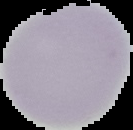
Summary:
  - Preparation: thin blood film
  - Image size: 133×130 pixels
  - Image type: cell region segmented out of the field of view; surrounding area masked to black
  - Result: no Plasmodium parasites seen